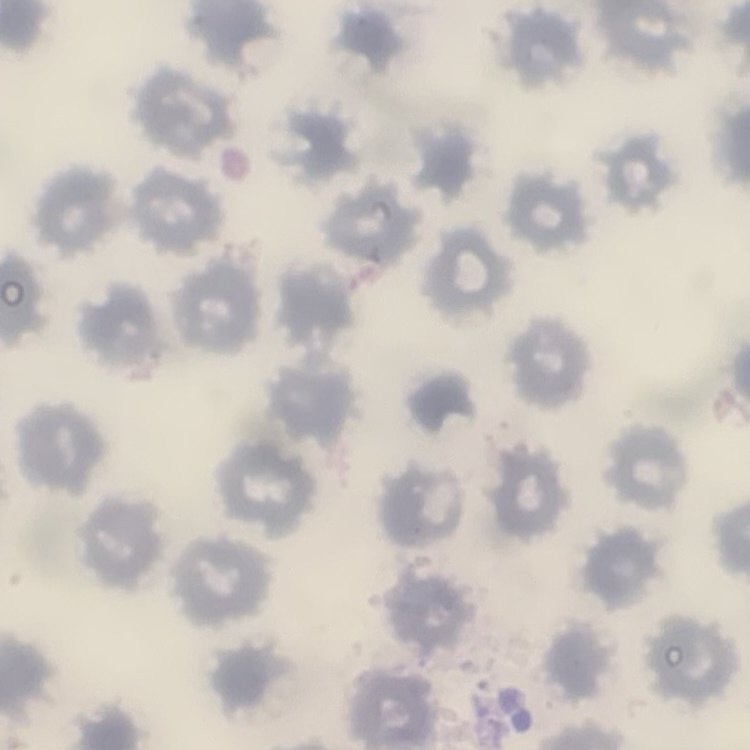

The erythrocytes show no rouleaux formation. One tile cut from a larger photomicrograph. Thin peripheral smear. Stained with either Field's or Giemsa.